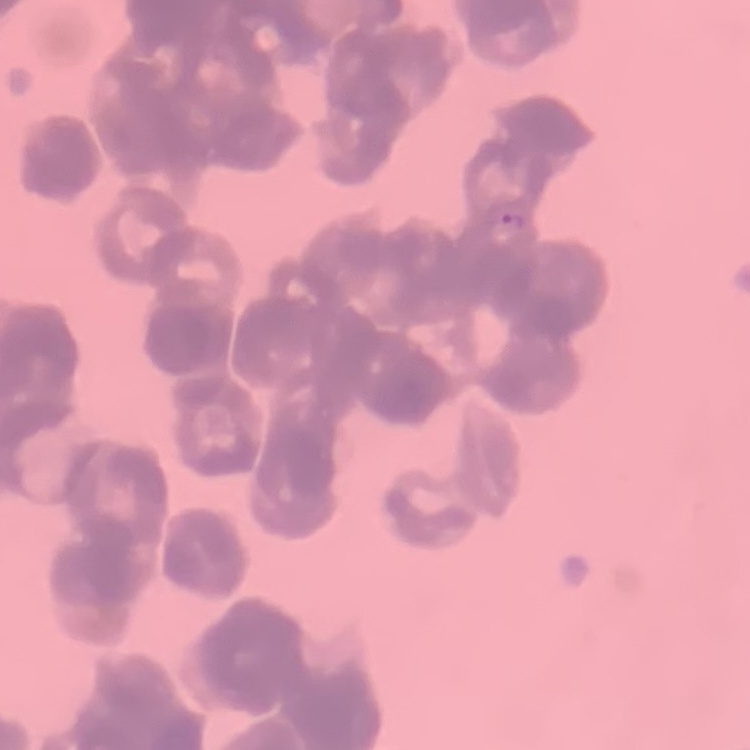
Summary:
  - Erythrocyte morphology: rouleaux formation
  - Stain: Field's or Giemsa
  - Preparation: thin blood smear
  - Image type: one tile cut from a larger photomicrograph